Draw a bounding box around every Plasmodium parasite, every leukocyte, and every artifact (stain precipitate or debris).
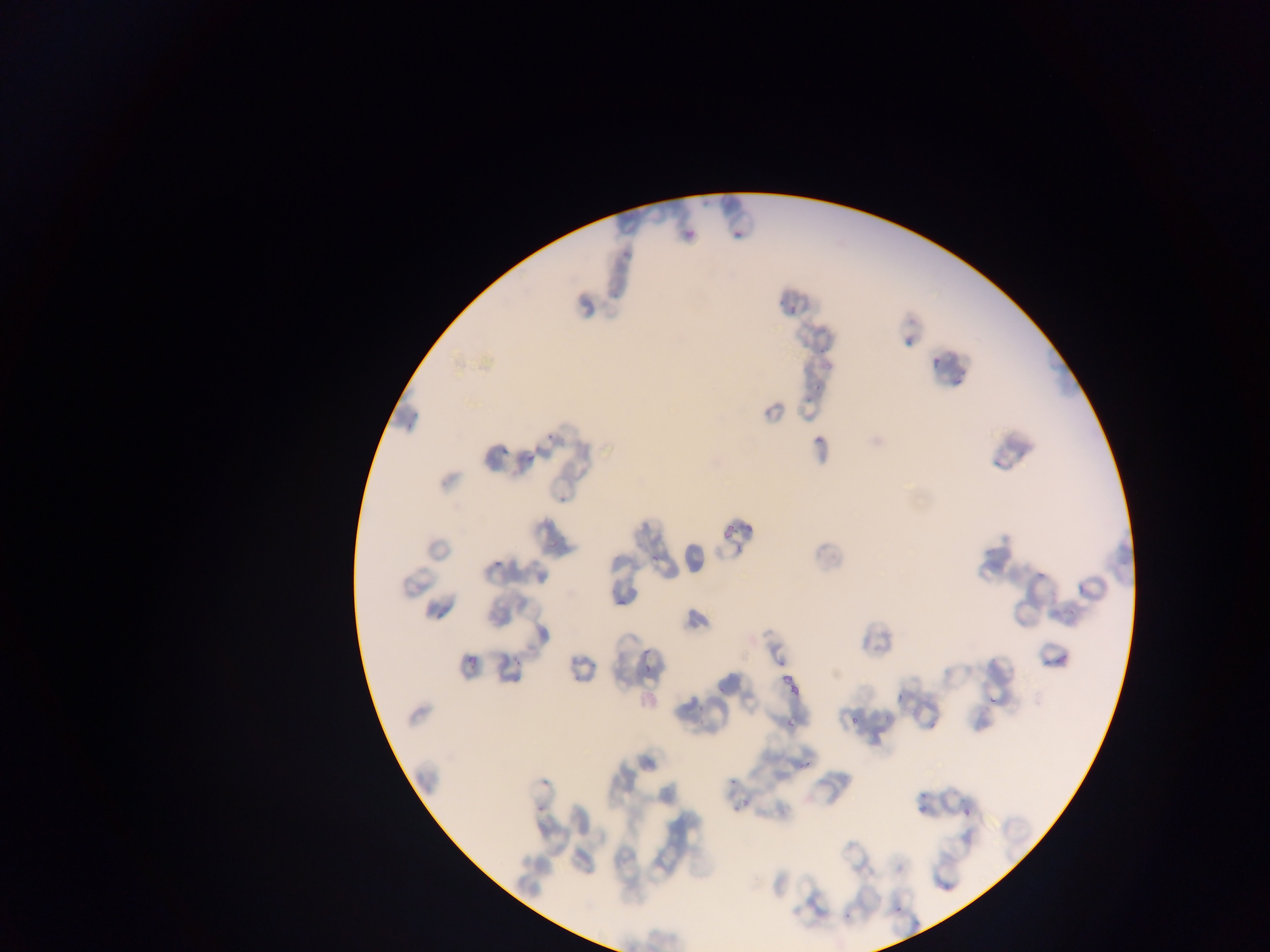

Approximate bounding boxes as left top right bottom in pixels.
Plasmodium parasites: 778 292 810 330; 930 349 946 372; 810 378 832 393; 794 393 805 404; 495 440 521 458; 651 541 670 563; 489 546 506 574; 1036 569 1044 582; 618 597 629 615; 635 646 665 666; 457 650 478 665; 1040 657 1056 673; 642 665 657 673; 776 670 792 688; 788 682 804 698; 889 684 907 703; 985 693 1004 707; 846 705 867 733; 778 717 792 733; 794 759 814 774; 534 773 551 790; 721 777 739 787; 726 796 753 819; 909 800 926 824; 957 804 973 822; 532 806 543 817; 890 888 919 921; 839 898 861 925.
No leukocytes observed.

Image is 1270×952 pixels. One field of view. Thin blood smear. Mobile-phone photograph taken through the microscope. Collected in Ghana.